Classify this cell by malaria status.
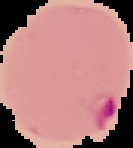
Parasitized.

Summary:
  - Preparation: thin blood smear
  - Image type: segmented cell region on a black background
  - Image size: 133×148 pixels